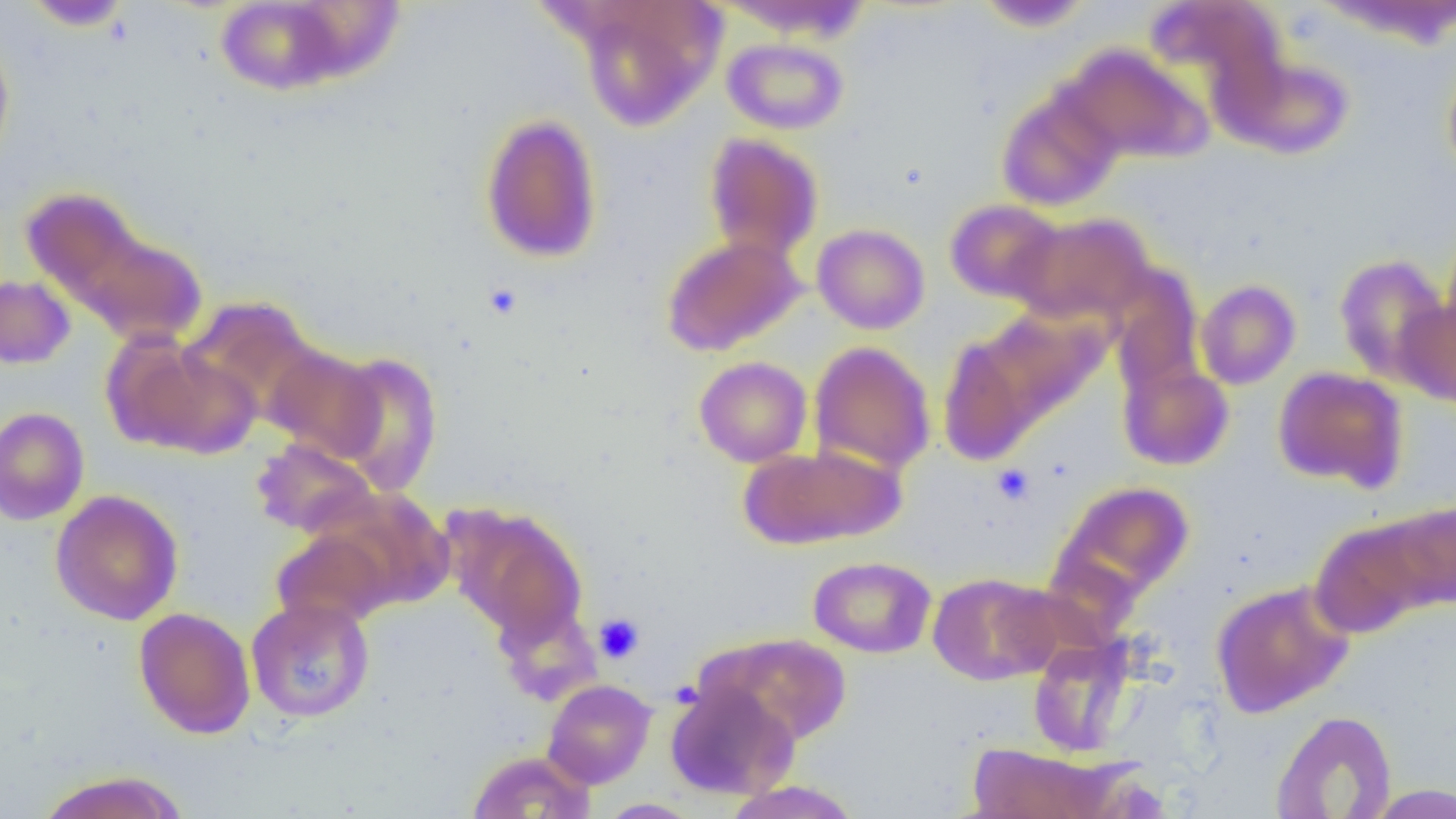
Summary:
  - Coordinate format: approximate bounding boxes as named x1/y1/x2/y2 corners in pixels
  - Uninfected red blood cell locations: (x1=21, y1=0, x2=134, y2=30), (x1=216, y1=0, x2=347, y2=95), (x1=979, y1=1, x2=1093, y2=32), (x1=1147, y1=1, x2=1286, y2=98), (x1=577, y1=2, x2=723, y2=130), (x1=0, y1=35, x2=15, y2=171), (x1=722, y1=37, x2=849, y2=135), (x1=1061, y1=45, x2=1210, y2=164), (x1=1231, y1=54, x2=1354, y2=160), (x1=1442, y1=64, x2=1456, y2=179), (x1=996, y1=89, x2=1122, y2=212), (x1=479, y1=113, x2=603, y2=264), (x1=703, y1=133, x2=823, y2=262), (x1=18, y1=185, x2=150, y2=304), (x1=31, y1=197, x2=207, y2=346), (x1=944, y1=199, x2=1065, y2=304), (x1=1010, y1=211, x2=1157, y2=327), (x1=812, y1=223, x2=930, y2=334), (x1=1440, y1=228, x2=1456, y2=356), (x1=661, y1=234, x2=806, y2=356), (x1=1333, y1=254, x2=1450, y2=383), (x1=1107, y1=268, x2=1203, y2=391), (x1=0, y1=274, x2=75, y2=369), (x1=1194, y1=279, x2=1301, y2=390), (x1=1395, y1=295, x2=1456, y2=408), (x1=181, y1=296, x2=325, y2=426), (x1=973, y1=307, x2=1108, y2=426), (x1=936, y1=332, x2=1043, y2=466), (x1=104, y1=335, x2=259, y2=458), (x1=808, y1=341, x2=936, y2=473), (x1=263, y1=345, x2=385, y2=463), (x1=328, y1=351, x2=444, y2=494), (x1=694, y1=356, x2=812, y2=467), (x1=1117, y1=359, x2=1235, y2=471), (x1=1272, y1=367, x2=1407, y2=491), (x1=0, y1=406, x2=90, y2=526), (x1=251, y1=437, x2=379, y2=538), (x1=739, y1=444, x2=904, y2=550), (x1=1053, y1=481, x2=1194, y2=603), (x1=50, y1=489, x2=184, y2=626), (x1=316, y1=490, x2=453, y2=612), (x1=1385, y1=500, x2=1456, y2=608), (x1=444, y1=503, x2=588, y2=646), (x1=1309, y1=517, x2=1440, y2=640), (x1=272, y1=528, x2=394, y2=629), (x1=808, y1=556, x2=936, y2=658), (x1=927, y1=573, x2=1058, y2=685), (x1=1210, y1=580, x2=1354, y2=718), (x1=245, y1=597, x2=375, y2=723), (x1=493, y1=602, x2=601, y2=706), (x1=134, y1=606, x2=256, y2=739), (x1=708, y1=633, x2=851, y2=746), (x1=1028, y1=636, x2=1137, y2=757), (x1=542, y1=678, x2=657, y2=788), (x1=664, y1=680, x2=799, y2=800), (x1=1271, y1=710, x2=1397, y2=818), (x1=967, y1=742, x2=1119, y2=818), (x1=466, y1=749, x2=596, y2=818), (x1=36, y1=769, x2=189, y2=819), (x1=723, y1=780, x2=862, y2=819), (x1=1366, y1=784, x2=1456, y2=818), (x1=595, y1=798, x2=703, y2=818)
  - Platelet locations: (x1=484, y1=282, x2=523, y2=320), (x1=992, y1=464, x2=1035, y2=505), (x1=593, y1=613, x2=645, y2=664)
  - Slide-level diagnosis: no evidence of blood parasites
  - Preparation: thin blood film
  - Field of view: single
  - Magnification: 1000x
  - Image size: 1456×819 pixels
  - Modality: light microscopy